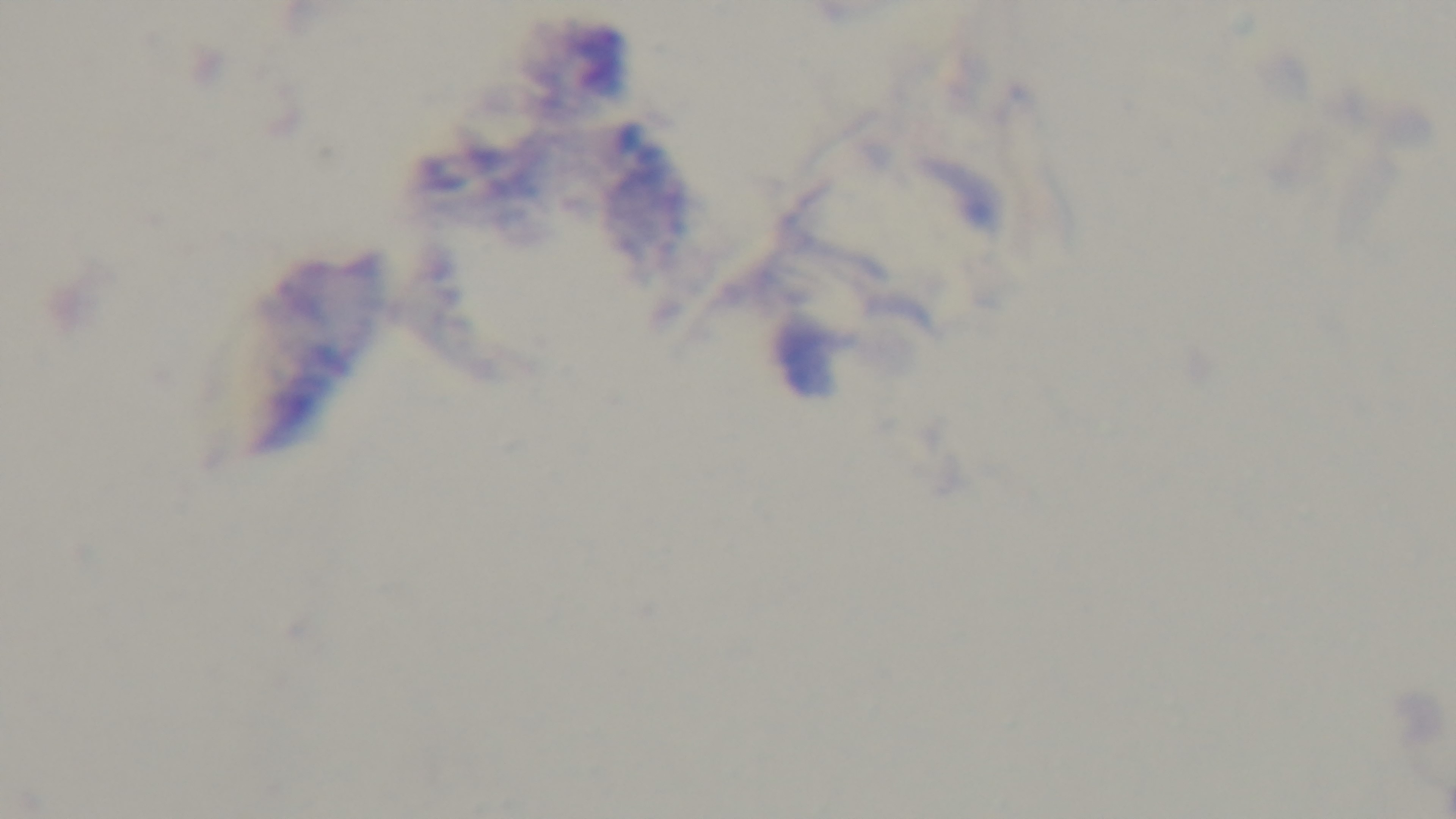

malaria status = uninfected
preparation = thick blood film
stain = Giemsa
objective = 100x oil immersion
modality = light microscopy
field of view = single
capture = mounted 4K digital camera